Classify this cell by malaria status.
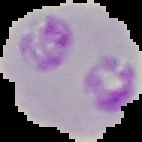

Parasitized.

{
  "image_type": "segmented cell region with the area outside set to black",
  "preparation": "thin blood film",
  "image_size": "142×142 pixels"
}